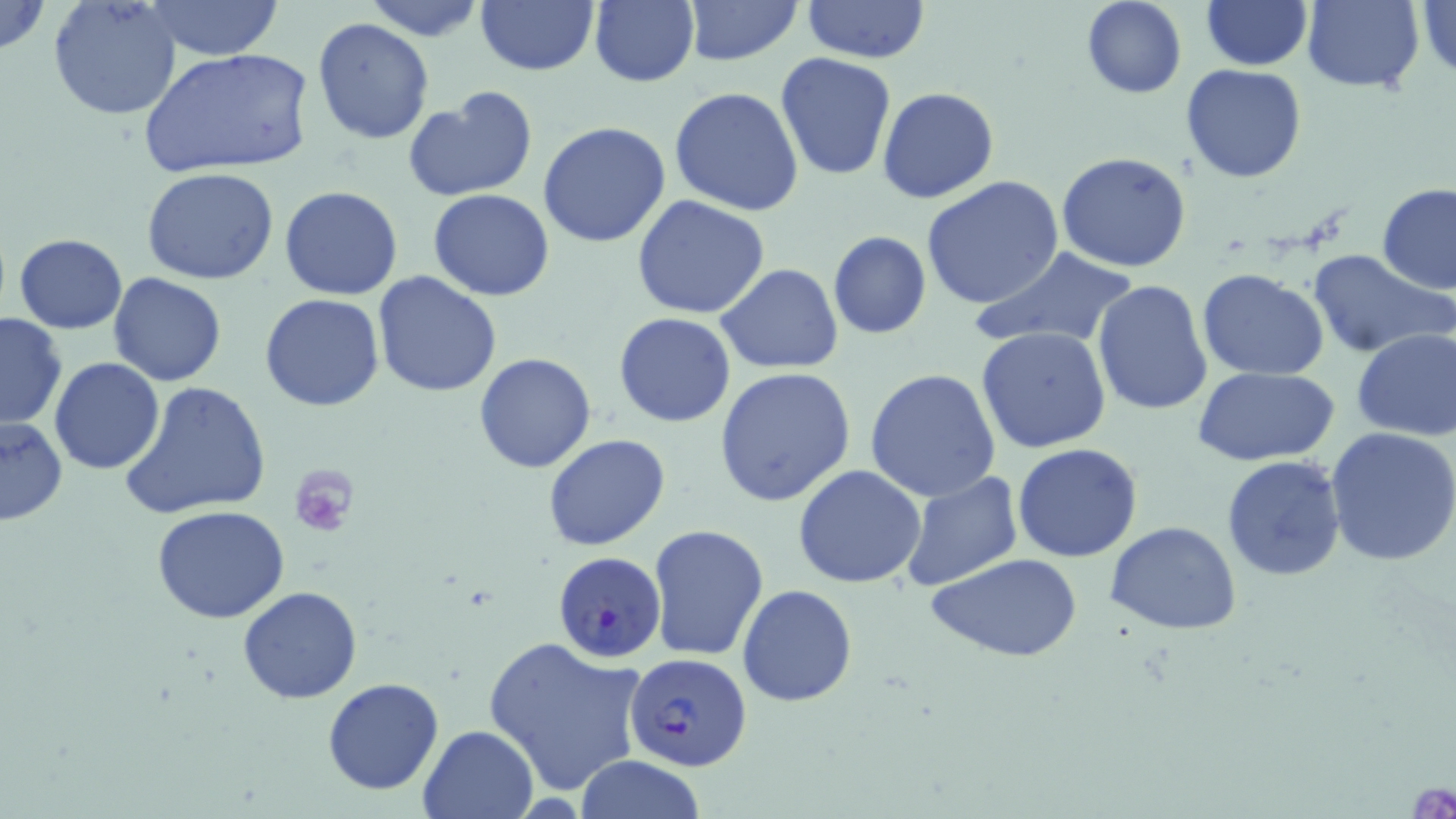

Plasmodium falciparum-infected red blood cell locations = approximate bounding boxes as (x1,y1)-(x2,y2) corner pairs in pixels: (552,551)-(668,664), (624,652)-(753,774)
slide-level diagnosis = Plasmodium falciparum
preparation = thin blood film
platelet locations = approximate bounding boxes as (x1,y1)-(x2,y2) corner pairs in pixels: (289,464)-(358,538)
image size = 1456×819 pixels
stain = May-Grünwald-Giemsa
modality = light microscopy
field of view = one of a larger specimen
uninfected red blood cell locations = approximate bounding boxes as (x1,y1)-(x2,y2) corner pairs in pixels: (0,0)-(50,59), (47,0)-(183,120), (475,0)-(599,77), (682,0)-(801,66), (803,0)-(929,65), (1081,0)-(1186,99), (1200,0)-(1311,70), (1300,0)-(1426,92), (141,1)-(285,60), (1414,1)-(1456,81), (360,2)-(491,42), (588,2)-(699,87), (41,18)-(269,146), (312,18)-(435,143), (142,48)-(312,179), (776,55)-(896,180), (1181,64)-(1307,184), (670,86)-(805,216), (877,86)-(999,203), (403,89)-(537,203), (539,121)-(671,248), (1057,151)-(1192,273), (927,166)-(1184,292), (140,168)-(280,284), (921,176)-(1065,310), (1376,183)-(1456,295), (280,186)-(403,299), (428,188)-(554,302), (631,194)-(770,319), (827,232)-(930,339), (14,233)-(126,332), (971,247)-(1141,350), (1306,249)-(1453,360), (717,263)-(844,375), (1197,268)-(1329,382), (372,270)-(502,398), (108,272)-(228,386), (1091,279)-(1212,416), (260,293)-(385,411), (0,310)-(68,429), (612,313)-(736,428), (976,326)-(1113,453), (1351,327)-(1456,442), (475,353)-(596,474), (49,358)-(164,474), (1192,366)-(1340,465), (715,367)-(858,507), (865,368)-(1002,504), (120,381)-(270,521), (0,415)-(69,526), (1327,426)-(1456,566), (543,434)-(670,550), (1011,443)-(1143,563), (1221,454)-(1347,582), (794,464)-(927,588), (898,470)-(1023,593), (151,505)-(291,623), (1105,521)-(1243,636), (647,524)-(768,660), (926,552)-(1084,664), (737,584)-(857,705), (237,586)-(363,703), (482,634)-(648,795), (322,677)-(444,796), (418,724)-(540,818), (571,756)-(710,818)
magnification = 1000x